Assess this cell for malaria.
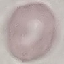
It is uninfected.

{
  "image_type": "cell patch, automatically extracted from a larger field of view and resized to 64 × 64 pixels",
  "stain": "Giemsa",
  "capture": "smartphone through the microscope eyepiece",
  "preparation": "thin blood film"
}